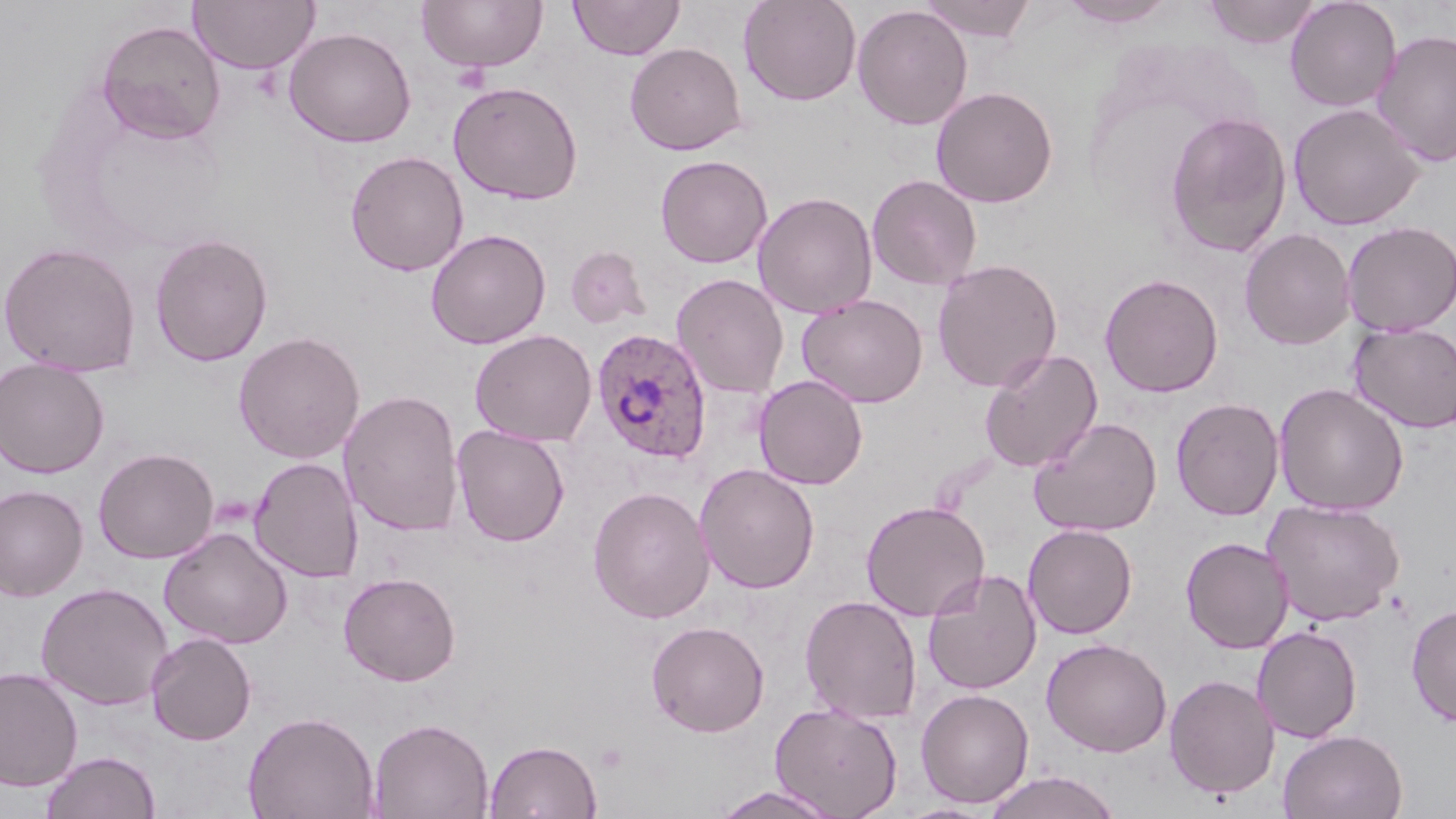

{
  "plasmodium_ovale_infected_red_blood_cell_locations": "approximate bounding boxes as (x1,y1)-(x2,y2) corner pairs in pixels: (591,327)-(712,464)",
  "slide_level_diagnosis": "Plasmodium ovale",
  "stain": "May-Grünwald-Giemsa",
  "image_size": "1456×819 pixels",
  "preparation": "thin blood film",
  "modality": "light microscopy",
  "field_of_view": "single",
  "uninfected_red_blood_cell_locations": "approximate bounding boxes as (x1,y1)-(x2,y2) corner pairs in pixels: (189,0)-(319,74), (416,0)-(548,74), (568,0)-(685,60), (739,0)-(862,107), (917,0)-(1038,42), (1202,0)-(1321,48), (1285,0)-(1402,112), (1058,1)-(1178,28), (852,4)-(974,130), (96,19)-(226,145), (283,27)-(417,147), (1371,27)-(1456,169), (625,42)-(746,155), (447,80)-(584,205), (930,86)-(1058,207), (1287,102)-(1425,231), (1164,111)-(1293,259), (345,150)-(469,276), (655,154)-(773,268), (866,174)-(982,291), (753,191)-(877,319), (1341,220)-(1456,337), (1239,227)-(1356,350), (425,229)-(551,349), (149,232)-(273,367), (0,241)-(141,377), (565,246)-(651,329), (932,258)-(1063,393), (671,272)-(790,399), (1100,273)-(1223,397), (797,294)-(928,408), (1347,323)-(1456,433), (470,329)-(597,446), (233,331)-(365,464), (979,348)-(1103,473), (0,357)-(110,478), (753,375)-(869,490), (1273,383)-(1410,516), (338,389)-(464,536), (1170,397)-(1285,521), (1028,416)-(1162,537), (452,424)-(570,547), (93,447)-(219,563), (248,457)-(363,583), (695,463)-(820,594), (0,484)-(88,601), (588,486)-(715,623), (1263,498)-(1405,626), (860,500)-(990,621), (1023,523)-(1137,639), (158,526)-(293,649), (1180,536)-(1294,654), (922,569)-(1043,695), (339,571)-(461,686), (36,582)-(173,710), (800,594)-(922,724), (1406,603)-(1456,727), (646,620)-(769,737), (1252,625)-(1363,743), (146,632)-(257,745), (1041,637)-(1172,757), (0,667)-(83,792), (1163,673)-(1279,799), (915,688)-(1035,808), (769,702)-(904,818), (241,710)-(380,819), (368,716)-(493,819), (1277,729)-(1408,819), (485,739)-(602,818), (40,750)-(161,819), (983,769)-(1122,819), (712,785)-(844,819)",
  "magnification": "1000x"
}